State the blood parasite species.
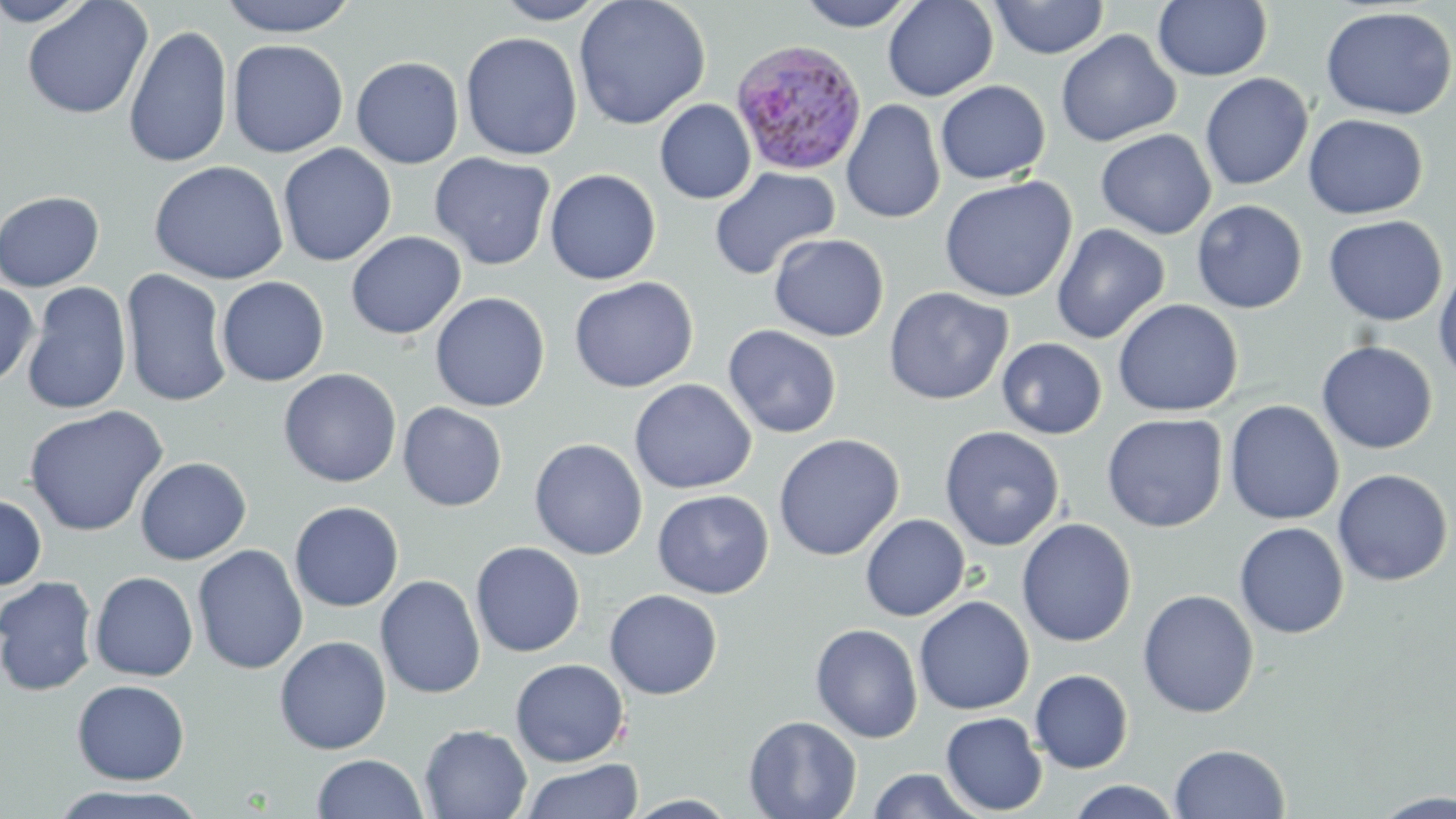

Plasmodium ovale.

Approximate bounding boxes as named x1/y1/x2/y2 corners in pixels. Uninfected red blood cell locations: (x1=0, y1=0, x2=98, y2=27), (x1=20, y1=0, x2=154, y2=120), (x1=217, y1=0, x2=360, y2=37), (x1=492, y1=0, x2=610, y2=24), (x1=573, y1=0, x2=711, y2=130), (x1=794, y1=0, x2=919, y2=31), (x1=883, y1=0, x2=998, y2=101), (x1=990, y1=0, x2=1109, y2=59), (x1=1153, y1=1, x2=1272, y2=81), (x1=1320, y1=6, x2=1456, y2=120), (x1=123, y1=24, x2=233, y2=168), (x1=1055, y1=29, x2=1181, y2=148), (x1=461, y1=32, x2=583, y2=161), (x1=227, y1=39, x2=348, y2=158), (x1=351, y1=56, x2=464, y2=169), (x1=1199, y1=72, x2=1314, y2=191), (x1=935, y1=81, x2=1051, y2=184), (x1=655, y1=99, x2=756, y2=204), (x1=841, y1=99, x2=945, y2=224), (x1=1303, y1=114, x2=1428, y2=219), (x1=1095, y1=129, x2=1216, y2=240), (x1=278, y1=143, x2=397, y2=267), (x1=429, y1=152, x2=556, y2=271), (x1=149, y1=160, x2=289, y2=284), (x1=709, y1=167, x2=839, y2=281), (x1=544, y1=169, x2=662, y2=285), (x1=938, y1=175, x2=1077, y2=303), (x1=0, y1=190, x2=105, y2=292), (x1=1191, y1=200, x2=1308, y2=314), (x1=1323, y1=215, x2=1447, y2=326), (x1=1051, y1=223, x2=1171, y2=344), (x1=345, y1=231, x2=467, y2=340), (x1=769, y1=233, x2=890, y2=342), (x1=1433, y1=263, x2=1456, y2=385), (x1=119, y1=269, x2=233, y2=408), (x1=216, y1=276, x2=330, y2=387), (x1=568, y1=276, x2=699, y2=393), (x1=0, y1=280, x2=39, y2=388), (x1=21, y1=281, x2=133, y2=416), (x1=884, y1=286, x2=1013, y2=405), (x1=429, y1=291, x2=550, y2=412), (x1=1111, y1=298, x2=1244, y2=417), (x1=722, y1=324, x2=842, y2=439), (x1=997, y1=337, x2=1107, y2=439), (x1=1316, y1=341, x2=1438, y2=454), (x1=278, y1=368, x2=402, y2=488), (x1=629, y1=378, x2=757, y2=494), (x1=1225, y1=400, x2=1344, y2=525), (x1=397, y1=402, x2=507, y2=511), (x1=23, y1=405, x2=169, y2=536), (x1=1102, y1=413, x2=1228, y2=533), (x1=939, y1=425, x2=1065, y2=551), (x1=773, y1=433, x2=904, y2=561), (x1=529, y1=438, x2=648, y2=560), (x1=134, y1=457, x2=252, y2=565), (x1=1332, y1=468, x2=1453, y2=587), (x1=653, y1=490, x2=774, y2=598), (x1=0, y1=493, x2=47, y2=591), (x1=289, y1=500, x2=404, y2=612), (x1=860, y1=514, x2=971, y2=621), (x1=1016, y1=518, x2=1138, y2=647), (x1=1233, y1=522, x2=1349, y2=639), (x1=470, y1=541, x2=586, y2=657), (x1=192, y1=544, x2=308, y2=674), (x1=90, y1=571, x2=198, y2=681), (x1=375, y1=575, x2=486, y2=699), (x1=0, y1=576, x2=99, y2=697), (x1=1137, y1=588, x2=1259, y2=718), (x1=604, y1=589, x2=723, y2=700), (x1=914, y1=595, x2=1034, y2=715), (x1=810, y1=623, x2=923, y2=743), (x1=274, y1=636, x2=391, y2=755), (x1=510, y1=659, x2=629, y2=767), (x1=1029, y1=669, x2=1134, y2=774), (x1=72, y1=679, x2=190, y2=784), (x1=940, y1=712, x2=1048, y2=816), (x1=744, y1=715, x2=862, y2=819), (x1=419, y1=724, x2=533, y2=819), (x1=1169, y1=743, x2=1290, y2=819), (x1=311, y1=753, x2=427, y2=818), (x1=520, y1=759, x2=643, y2=819), (x1=866, y1=768, x2=984, y2=818), (x1=1065, y1=780, x2=1184, y2=819), (x1=47, y1=786, x2=212, y2=819), (x1=1372, y1=791, x2=1456, y2=818). Plasmodium ovale-infected red blood cell locations: (x1=729, y1=38, x2=868, y2=176). May-Grünwald-Giemsa-stained preparation. Thin blood smear. 1000x magnification. Light microscopy. Image is 1456×819 pixels. One field of a larger specimen.